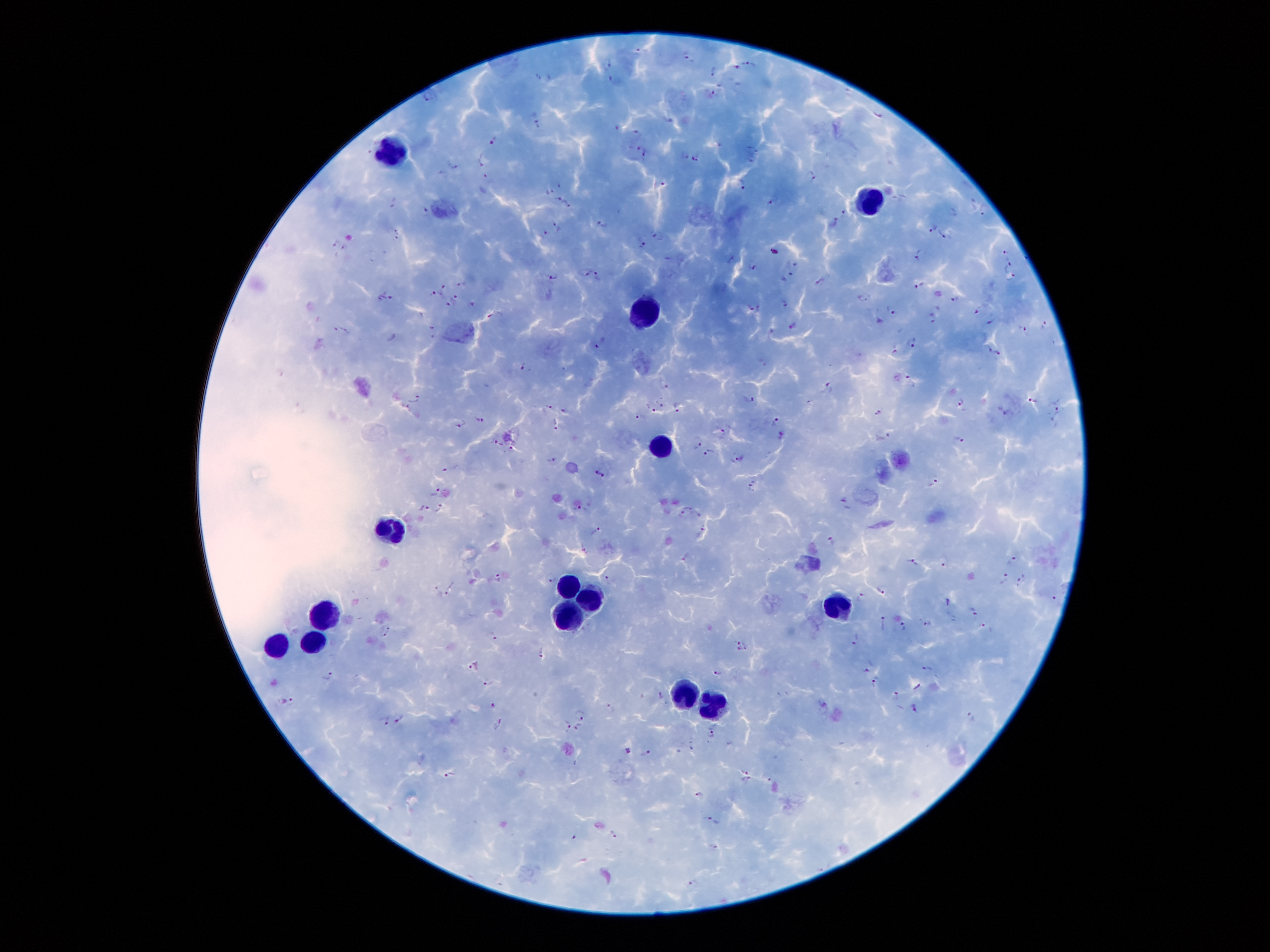 Approximate object centers, in pixels from the top-left corner. Leukocyte locations: (x=391, y=151), (x=870, y=202), (x=644, y=314), (x=660, y=445), (x=394, y=525), (x=564, y=586), (x=590, y=596), (x=838, y=607), (x=326, y=613), (x=564, y=617), (x=314, y=640), (x=276, y=642), (x=683, y=701), (x=714, y=705). Plasmodium parasite locations: (x=638, y=50), (x=687, y=53), (x=611, y=60), (x=749, y=62), (x=736, y=67), (x=714, y=70), (x=538, y=76), (x=549, y=76), (x=609, y=78), (x=713, y=92), (x=429, y=93), (x=876, y=113), (x=668, y=119), (x=538, y=122), (x=634, y=127), (x=615, y=129), (x=494, y=139), (x=637, y=145), (x=753, y=147), (x=646, y=154), (x=686, y=155), (x=484, y=158), (x=696, y=158), (x=751, y=159), (x=454, y=163), (x=441, y=173), (x=813, y=174), (x=485, y=177), (x=742, y=182), (x=661, y=184), (x=549, y=188), (x=557, y=198), (x=774, y=199), (x=972, y=199), (x=395, y=202), (x=569, y=203), (x=422, y=209), (x=983, y=210), (x=845, y=212), (x=602, y=223), (x=833, y=223), (x=557, y=227), (x=933, y=227), (x=545, y=233), (x=398, y=234), (x=943, y=234), (x=658, y=235), (x=642, y=244), (x=338, y=245), (x=918, y=252), (x=1006, y=253), (x=668, y=258), (x=731, y=258), (x=797, y=264), (x=752, y=265), (x=1008, y=266), (x=588, y=271), (x=789, y=272), (x=553, y=274), (x=600, y=274), (x=1010, y=277), (x=820, y=282), (x=460, y=283), (x=920, y=285), (x=441, y=286), (x=431, y=292), (x=388, y=295), (x=455, y=297), (x=956, y=298), (x=865, y=299), (x=473, y=301), (x=784, y=301), (x=449, y=304), (x=756, y=306), (x=979, y=307), (x=894, y=312), (x=933, y=318), (x=990, y=321), (x=793, y=325), (x=1045, y=325), (x=1021, y=327), (x=341, y=328), (x=432, y=328), (x=602, y=341), (x=912, y=341), (x=987, y=348), (x=895, y=352), (x=999, y=354), (x=764, y=361), (x=525, y=365), (x=910, y=379), (x=664, y=382), (x=831, y=387), (x=415, y=396), (x=749, y=399), (x=1034, y=400), (x=661, y=401), (x=959, y=401), (x=1057, y=402), (x=405, y=405), (x=549, y=406), (x=676, y=406), (x=651, y=407), (x=564, y=410), (x=879, y=410), (x=1006, y=411), (x=639, y=414), (x=480, y=415), (x=773, y=419), (x=556, y=422), (x=460, y=423), (x=723, y=430), (x=781, y=435), (x=885, y=435), (x=959, y=438), (x=498, y=443), (x=698, y=443), (x=511, y=446), (x=708, y=451), (x=739, y=457), (x=552, y=459), (x=452, y=467), (x=600, y=473), (x=755, y=484), (x=934, y=484), (x=436, y=490), (x=423, y=507), (x=577, y=507), (x=688, y=508), (x=439, y=509), (x=681, y=513), (x=697, y=514), (x=595, y=531), (x=700, y=532), (x=831, y=540), (x=584, y=549), (x=685, y=557), (x=1012, y=559), (x=946, y=561), (x=913, y=562), (x=607, y=577), (x=1004, y=577), (x=498, y=578), (x=549, y=580), (x=1020, y=580), (x=882, y=588), (x=450, y=589), (x=859, y=594), (x=1055, y=598), (x=947, y=602), (x=973, y=610), (x=883, y=622), (x=926, y=622), (x=983, y=624), (x=903, y=626), (x=388, y=627), (x=386, y=635), (x=493, y=636), (x=856, y=639), (x=739, y=642), (x=747, y=647), (x=738, y=648), (x=541, y=652), (x=928, y=665), (x=475, y=666), (x=866, y=671), (x=720, y=672), (x=329, y=675), (x=874, y=681), (x=488, y=683), (x=918, y=685), (x=896, y=693), (x=661, y=694), (x=291, y=700), (x=822, y=702), (x=495, y=705), (x=915, y=707), (x=611, y=708), (x=581, y=715), (x=973, y=717), (x=400, y=719), (x=387, y=721), (x=500, y=723), (x=566, y=725), (x=578, y=727), (x=713, y=733), (x=627, y=751), (x=646, y=753), (x=745, y=769), (x=451, y=773), (x=748, y=780), (x=700, y=796), (x=707, y=817), (x=614, y=832), (x=715, y=847), (x=695, y=882). Image is 1270×952 pixels. One field from this slide. Giemsa-stained preparation. Patient malaria status: infected with Plasmodium falciparum. Photographed through the microscope eyepiece with a smartphone camera. Thick blood film. 100x magnification.